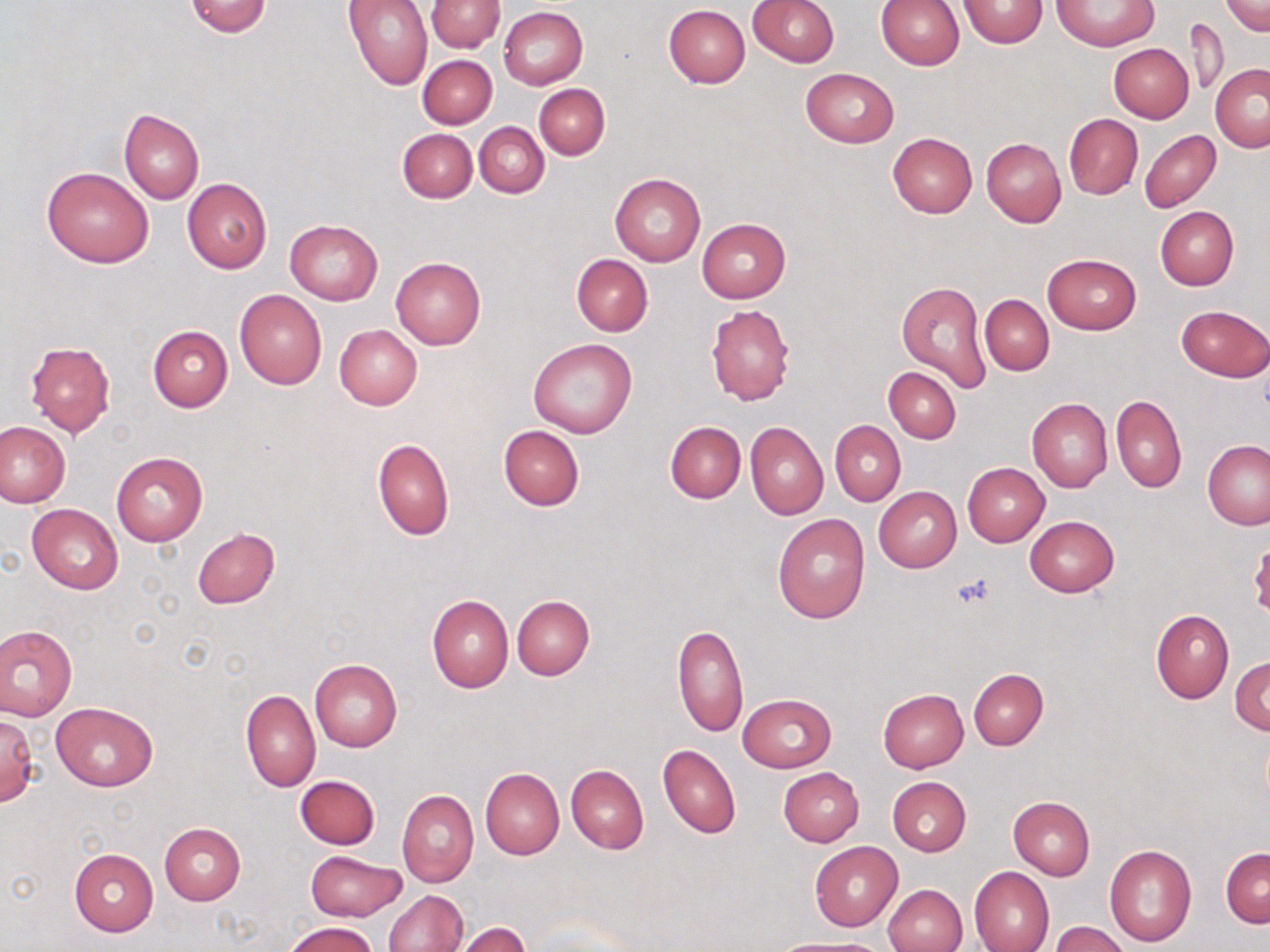
{
  "slide_level_diagnosis": "negative for blood parasites",
  "uninfected_red_blood_cell_locations": "approximate bounding boxes as (x1,y1)-(x2,y2) corner pairs in pixels: (184,0)-(273,37), (345,0)-(432,90), (748,0)-(840,68), (959,0)-(1048,47), (1052,0)-(1156,50), (1220,0)-(1269,36), (426,1)-(504,52), (876,1)-(964,70), (663,4)-(750,88), (498,6)-(588,89), (1183,16)-(1230,98), (1108,44)-(1194,123), (418,54)-(496,128), (1210,64)-(1270,151), (800,68)-(898,147), (534,84)-(610,160), (119,109)-(204,203), (1064,115)-(1143,199), (475,122)-(550,198), (397,128)-(478,203), (1139,129)-(1221,213), (887,133)-(978,218), (981,137)-(1066,227), (42,166)-(154,268), (609,173)-(705,266), (182,178)-(272,274), (1154,206)-(1239,290), (697,217)-(790,302), (285,219)-(384,304), (571,253)-(653,336), (1043,253)-(1141,334), (391,256)-(487,349), (897,280)-(993,390), (234,290)-(328,389), (980,295)-(1053,375), (706,303)-(796,405), (1176,305)-(1270,381), (334,325)-(422,409), (147,326)-(233,412), (529,337)-(636,437), (25,340)-(115,438), (883,367)-(961,443), (1112,395)-(1186,492), (1026,398)-(1113,493), (830,420)-(906,505), (665,421)-(746,504), (745,421)-(828,520), (0,422)-(70,507), (498,425)-(585,511), (372,439)-(454,540), (1203,441)-(1270,530), (111,452)-(206,546), (962,462)-(1049,546), (874,487)-(961,572), (27,503)-(123,594), (773,514)-(870,623), (1025,515)-(1119,597), (192,528)-(281,609), (427,594)-(513,692), (512,595)-(594,679), (1151,609)-(1234,703), (0,623)-(77,720), (671,625)-(749,737), (309,656)-(403,752), (1230,657)-(1270,734), (968,668)-(1048,750), (241,689)-(321,791), (877,689)-(967,773), (737,693)-(837,772), (49,702)-(158,791), (0,712)-(39,807), (659,745)-(740,838), (566,764)-(648,854), (480,767)-(564,859), (779,767)-(864,846), (294,775)-(380,850), (887,776)-(971,856), (397,789)-(478,887), (1008,795)-(1095,879), (160,823)-(245,905), (809,841)-(903,931), (1103,843)-(1197,947), (1220,847)-(1270,926), (70,849)-(158,936), (305,849)-(405,922), (969,867)-(1054,952), (881,884)-(968,952), (385,889)-(469,952), (1049,921)-(1132,952), (283,922)-(377,952), (451,922)-(530,952), (773,938)-(891,952)",
  "image_size": "1270×952 pixels",
  "platelet_locations": "approximate bounding boxes as (x1,y1)-(x2,y2) corner pairs in pixels: (950,573)-(998,610)",
  "magnification": "1000x",
  "preparation": "thin blood smear",
  "stain": "May-Grünwald-Giemsa",
  "modality": "optical microscopy",
  "field_of_view": "single"
}